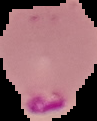

image type = cell region segmented out of the field of view; surrounding area masked to black
preparation = thin blood smear
image size = 97×121 pixels
result = Plasmodium parasites identified